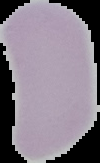
result = no malaria parasites seen
image size = 100×163 pixels
image type = segmented cell region with the area outside set to black
preparation = thin blood smear